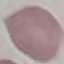

Malaria status: uninfected. Thin smear of blood. Acquired by smartphone through the microscope eyepiece. Giemsa-stained preparation. Automatically extracted cell patch, resized to 64 × 64 pixels.